Give the position of every leukocyte visible.
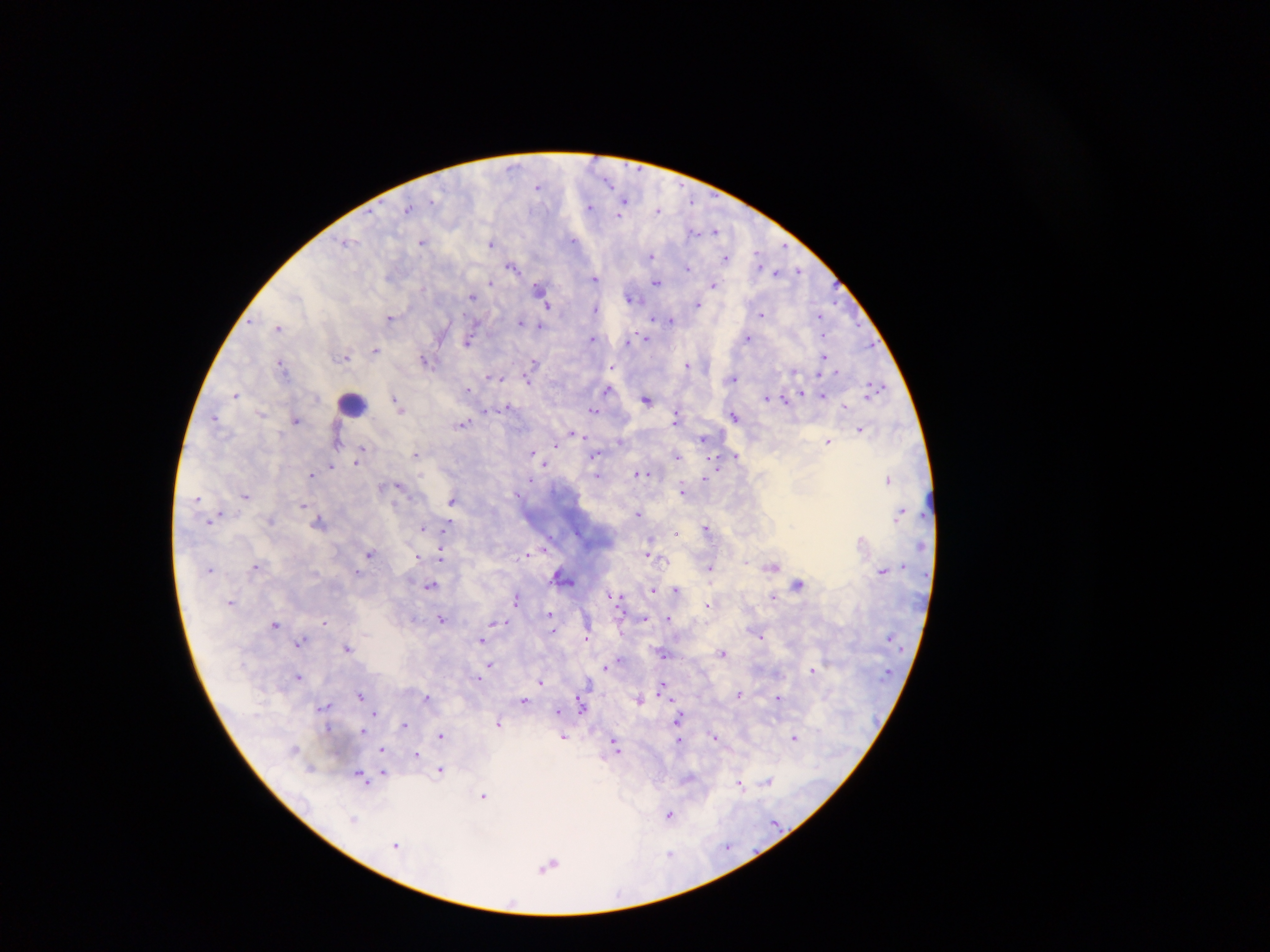
Approximate centers as x y in pixels.
Leukocytes: 353 403; 933 504.

{
  "capture": "mobile-phone photograph through a microscope",
  "malaria_parasite_locations": "approximate centers as x y in pixels: 609 182; 538 186; 625 200; 432 201; 693 202; 589 207; 408 208; 658 210; 619 216; 693 231; 715 231; 573 240; 345 242; 422 242; 491 243; 784 246; 758 254; 650 256; 726 258; 759 265; 513 266; 689 267; 798 270; 776 273; 595 278; 491 281; 657 281; 714 284; 539 287; 295 295; 472 296; 631 297; 697 304; 548 306; 596 309; 761 314; 819 315; 390 318; 653 319; 670 320; 521 321; 475 324; 540 326; 278 327; 592 337; 646 338; 747 338; 630 339; 467 343; 870 345; 376 351; 824 356; 346 357; 424 360; 534 362; 281 363; 687 365; 612 367; 794 371; 836 372; 819 376; 487 377; 495 377; 501 378; 733 378; 528 380; 875 388; 469 389; 608 389; 802 393; 823 394; 236 395; 784 398; 766 399; 647 400; 396 402; 400 407; 506 407; 845 407; 593 410; 486 411; 676 412; 734 416; 215 418; 676 418; 296 419; 462 423; 860 429; 576 435; 584 437; 703 438; 336 439; 620 441; 828 442; 555 446; 362 449; 532 452; 595 454; 736 455; 415 456; 677 456; 358 461; 545 463; 330 466; 311 474; 641 474; 597 475; 705 477; 888 479; 530 480; 398 485; 383 487; 682 490; 246 494; 198 497; 452 501; 303 505; 638 512; 901 512; 210 519; 319 521; 423 527; 445 527; 706 527; 677 533; 650 539; 369 553; 648 554; 442 555; 527 555; 418 557; 745 560; 903 566; 255 567; 772 567; 209 568; 710 569; 883 570; 357 571; 561 576; 568 581; 800 582; 430 585; 676 589; 653 590; 609 596; 773 596; 517 598; 619 598; 708 604; 550 614; 645 617; 669 617; 441 618; 325 620; 505 622; 276 624; 552 630; 761 636; 586 639; 482 640; 300 642; 348 649; 723 653; 664 654; 619 660; 489 663; 606 668; 812 669; 299 676; 478 677; 541 682; 662 688; 740 694; 360 695; 427 697; 778 697; 640 699; 524 700; 579 700; 325 705; 581 708; 374 711; 558 711; 679 717; 498 723; 404 725; 363 732; 441 735; 715 736; 563 737; 794 737; 680 742; 615 744; 382 750; 416 755; 311 768; 441 770; 384 773; 361 777; 688 777; 768 781; 739 783; 484 795; 669 815; 354 820; 396 844; 728 846; 670 853; 549 865",
  "preparation": "thick blood film",
  "image_size": "1270×952 pixels",
  "field_of_view": "single",
  "country": "Ghana"
}